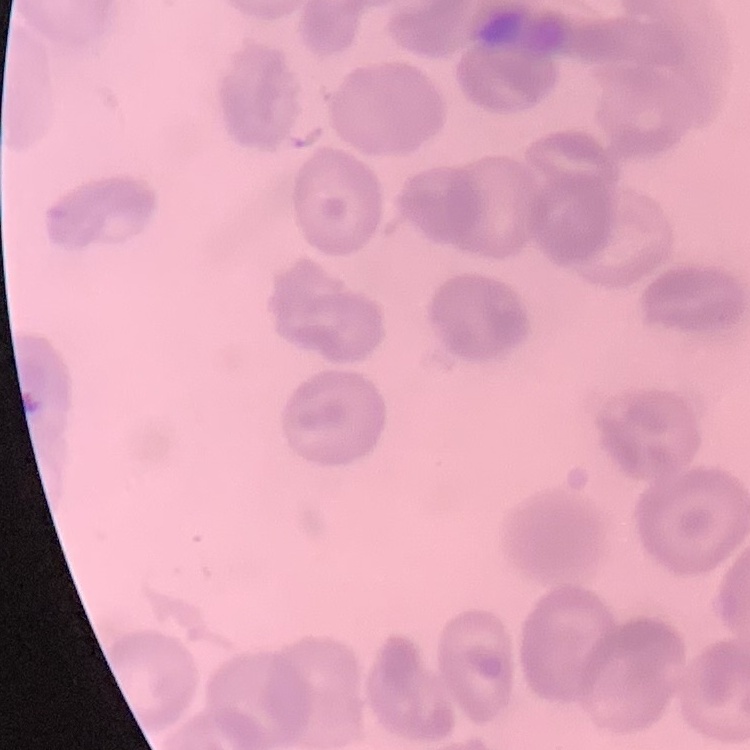

The erythrocytes show no rouleaux formation. Field's or Giemsa stain. Thin blood film. Square crop of a larger photomicrograph.